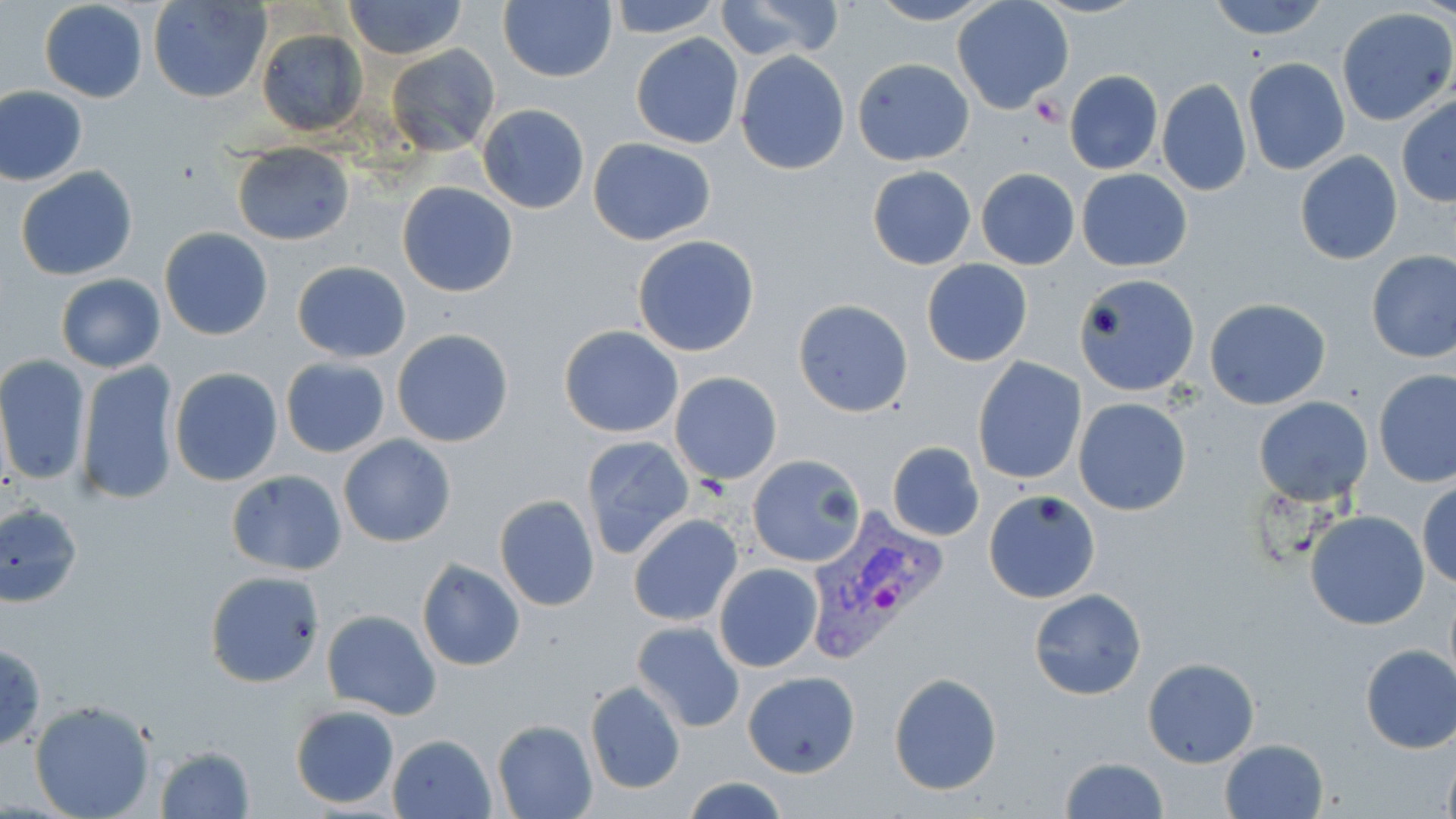

Approximate bounding boxes as (x1,y1)-(x2,y2) corner pairs in pixels. Uninfected red blood cell locations: (344,0)-(468,58), (607,0)-(724,38), (866,0)-(997,25), (1202,0)-(1332,41), (147,1)-(272,104), (499,1)-(616,83), (715,1)-(844,59), (952,1)-(1074,114), (39,2)-(148,103), (1337,8)-(1455,125), (256,29)-(366,134), (630,34)-(744,149), (386,44)-(500,156), (735,51)-(850,174), (1242,57)-(1350,175), (853,58)-(974,166), (1064,70)-(1162,174), (1157,78)-(1252,196), (0,87)-(88,186), (1396,96)-(1456,206), (477,103)-(589,213), (588,137)-(716,246), (232,144)-(355,245), (1294,150)-(1403,265), (15,164)-(138,281), (867,165)-(976,270), (1077,167)-(1192,271), (976,168)-(1080,270), (398,183)-(518,297), (159,228)-(273,341), (631,234)-(761,357), (1366,250)-(1456,363), (921,258)-(1033,367), (291,260)-(411,362), (56,273)-(165,372), (1075,277)-(1198,397), (794,299)-(914,418), (1205,299)-(1331,409), (559,325)-(684,438), (392,328)-(514,448), (0,356)-(89,486), (972,357)-(1087,485), (280,358)-(390,457), (75,361)-(181,506), (168,368)-(283,486), (1374,369)-(1456,488), (670,372)-(782,485), (1254,397)-(1373,506), (1075,399)-(1191,517), (338,435)-(456,548), (581,436)-(694,561), (887,441)-(984,542), (747,454)-(866,567), (226,470)-(347,575), (1417,480)-(1456,590), (986,491)-(1100,613), (494,495)-(600,613), (0,501)-(85,608), (1304,510)-(1430,630), (628,514)-(742,626), (416,559)-(525,671), (715,563)-(822,672), (204,570)-(326,688), (1029,589)-(1146,699), (321,609)-(441,719), (631,620)-(745,733), (0,641)-(47,753), (1359,645)-(1456,754), (1142,658)-(1261,768), (743,672)-(859,778), (888,674)-(1004,795), (585,680)-(686,794), (28,700)-(156,819), (290,704)-(400,809), (492,719)-(598,819), (388,733)-(496,818), (1219,739)-(1329,819), (152,744)-(256,819), (1439,749)-(1456,819), (1057,756)-(1167,818), (682,776)-(789,819). Plasmodium vivax-infected red blood cell locations: (803,503)-(950,664). Platelet locations: (1029,95)-(1067,128). Slide-level diagnosis: Plasmodium vivax. Thin blood film. Light microscopy. Single field of view. Captured at 1000x magnification. May-Grünwald-Giemsa stain. Image is 1456×819 pixels.